Assess this cell for malaria.
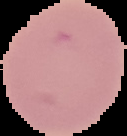
It is uninfected.

The area outside the segmented cell region is set to black. From a thin blood film. Image is 127×136 pixels.